Identify the parasite.
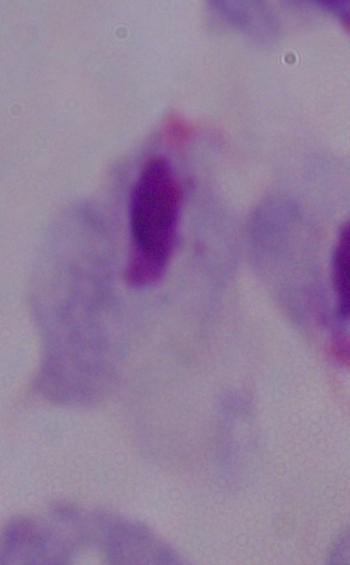
This is a trichomonad.

Summary:
  - Modality: micrograph
  - Magnification: 1000x